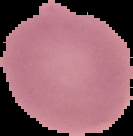
Summary:
  - Malaria status: uninfected
  - Image size: 133×136 pixels
  - Preparation: thin blood smear
  - Image type: segmented cell region on a black background